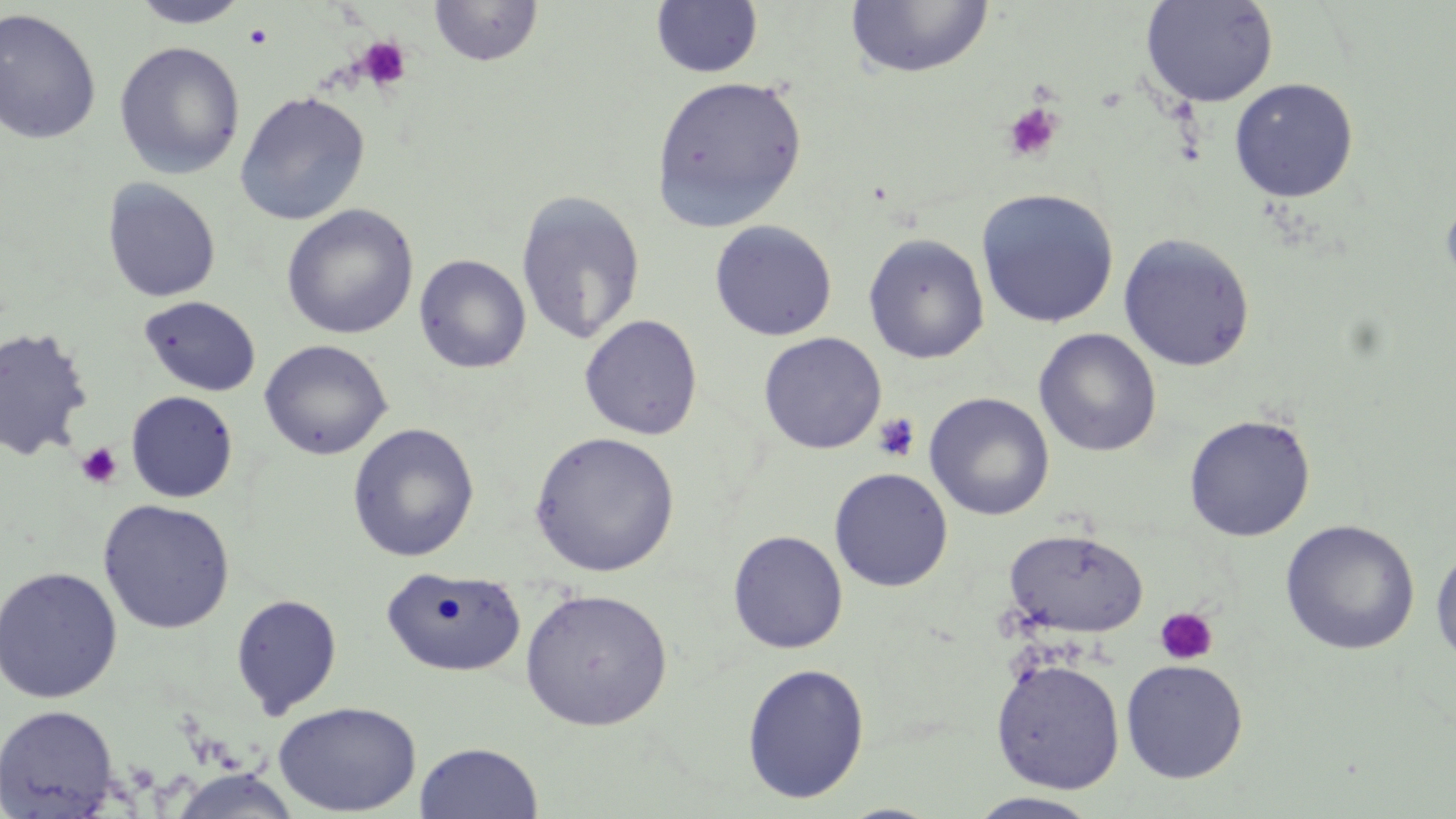

Approximate bounding boxes as named x1/y1/x2/y2 corners in pixels. Platelet locations: (x1=244, y1=23, x2=273, y2=49), (x1=355, y1=36, x2=412, y2=92), (x1=1001, y1=103, x2=1064, y2=163), (x1=873, y1=412, x2=921, y2=462), (x1=75, y1=441, x2=124, y2=489), (x1=1154, y1=606, x2=1219, y2=666). Uninfected red blood cell locations: (x1=1141, y1=0, x2=1279, y2=107), (x1=130, y1=1, x2=249, y2=28), (x1=429, y1=1, x2=543, y2=68), (x1=651, y1=1, x2=764, y2=79), (x1=845, y1=1, x2=995, y2=80), (x1=0, y1=8, x2=102, y2=145), (x1=113, y1=41, x2=246, y2=180), (x1=651, y1=74, x2=808, y2=231), (x1=1228, y1=77, x2=1359, y2=202), (x1=234, y1=91, x2=371, y2=226), (x1=102, y1=178, x2=221, y2=303), (x1=1439, y1=186, x2=1456, y2=298), (x1=515, y1=188, x2=647, y2=345), (x1=976, y1=188, x2=1119, y2=328), (x1=281, y1=204, x2=419, y2=340), (x1=709, y1=220, x2=837, y2=341), (x1=863, y1=232, x2=990, y2=364), (x1=1118, y1=232, x2=1256, y2=372), (x1=414, y1=254, x2=531, y2=374), (x1=139, y1=295, x2=261, y2=397), (x1=579, y1=314, x2=703, y2=440), (x1=0, y1=326, x2=93, y2=462), (x1=1034, y1=328, x2=1162, y2=457), (x1=758, y1=332, x2=886, y2=455), (x1=259, y1=339, x2=392, y2=460), (x1=126, y1=391, x2=238, y2=503), (x1=924, y1=392, x2=1055, y2=521), (x1=1184, y1=413, x2=1316, y2=542), (x1=347, y1=423, x2=480, y2=562), (x1=529, y1=431, x2=680, y2=577), (x1=829, y1=467, x2=953, y2=592), (x1=97, y1=499, x2=236, y2=634), (x1=1280, y1=519, x2=1420, y2=655), (x1=1004, y1=529, x2=1148, y2=638), (x1=728, y1=530, x2=848, y2=653), (x1=1430, y1=544, x2=1456, y2=668), (x1=0, y1=565, x2=123, y2=704), (x1=380, y1=566, x2=526, y2=678), (x1=520, y1=587, x2=673, y2=730), (x1=230, y1=593, x2=343, y2=718), (x1=991, y1=657, x2=1126, y2=793), (x1=1120, y1=659, x2=1249, y2=783), (x1=741, y1=662, x2=870, y2=803), (x1=272, y1=700, x2=422, y2=816), (x1=0, y1=703, x2=121, y2=818), (x1=414, y1=741, x2=543, y2=819), (x1=167, y1=768, x2=303, y2=819), (x1=965, y1=792, x2=1104, y2=819). Slide-level diagnosis: no evidence of blood parasites. Captured at 1000x magnification. Thin blood film. One field of a larger specimen. May-Grünwald-Giemsa-stained preparation. Image is 1456×819 pixels. Optical microscopy.